Name the blood parasite species.
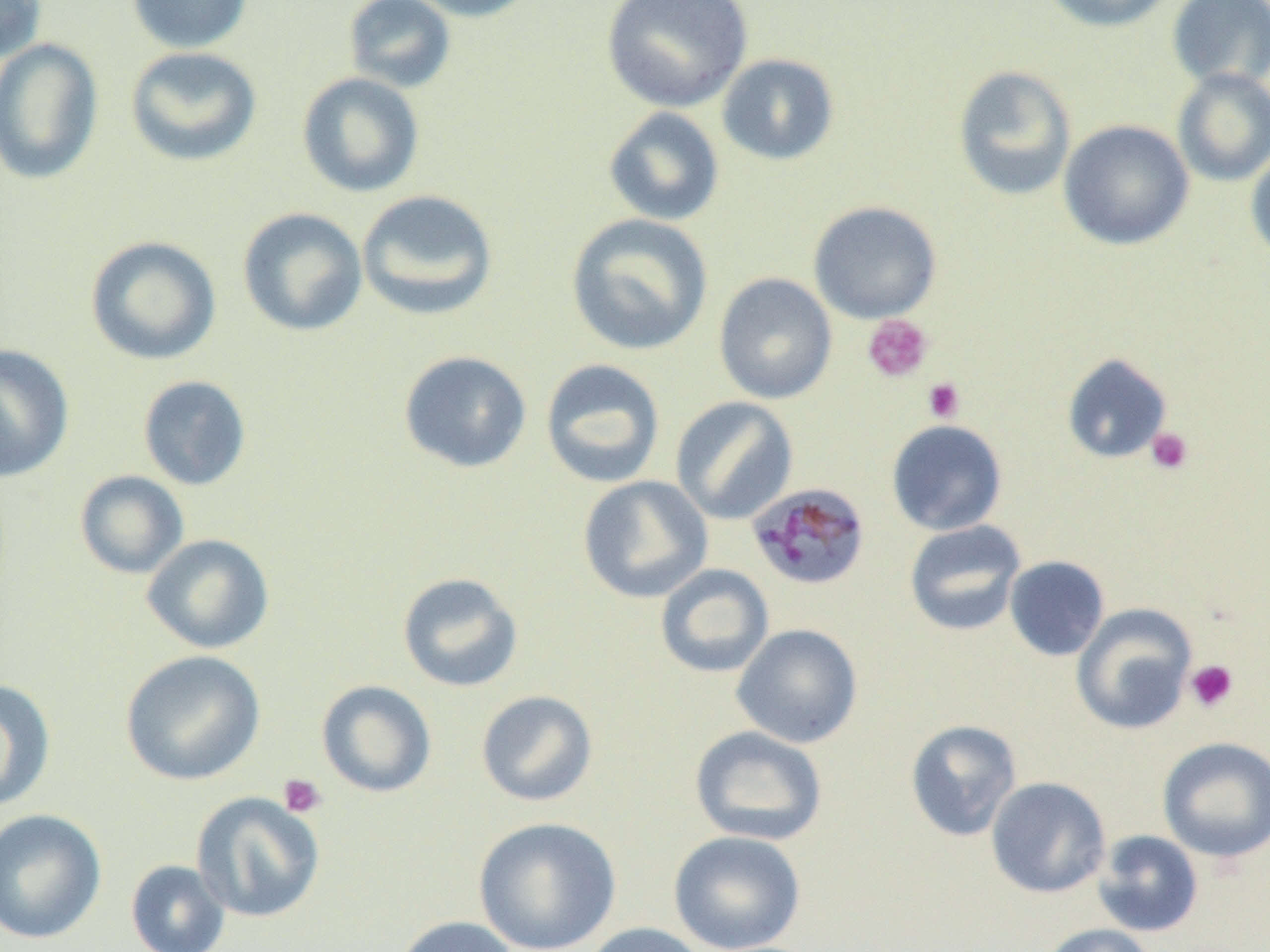
Plasmodium malariae.

Summary:
  - Coordinate format: approximate bounding boxes as (x1, y1, x2, y2) in pixels
  - Uninfected red blood cell locations: (0, 0, 47, 62), (127, 0, 252, 54), (342, 0, 457, 93), (407, 0, 541, 22), (601, 0, 753, 112), (1038, 0, 1175, 32), (1167, 0, 1270, 91), (0, 39, 104, 185), (125, 46, 262, 167), (717, 53, 840, 166), (952, 64, 1077, 201), (1172, 68, 1270, 187), (297, 72, 425, 198), (603, 107, 724, 226), (1058, 119, 1194, 251), (1246, 145, 1270, 265), (356, 189, 498, 321), (808, 200, 942, 324), (237, 207, 368, 337), (565, 213, 714, 356), (85, 235, 221, 365), (713, 272, 837, 404), (0, 344, 75, 483), (398, 350, 532, 474), (1062, 353, 1173, 464), (540, 358, 666, 488), (137, 375, 252, 491), (670, 396, 799, 525), (886, 419, 1007, 536), (74, 470, 189, 579), (577, 475, 713, 603), (904, 520, 1027, 636), (142, 534, 275, 654), (1004, 555, 1110, 662), (655, 564, 774, 679), (397, 572, 523, 693), (1071, 603, 1197, 734), (731, 623, 863, 749), (120, 650, 267, 786), (0, 678, 56, 813), (316, 680, 437, 798), (475, 690, 598, 806), (905, 719, 1022, 842), (689, 725, 828, 846), (1157, 737, 1270, 863), (985, 777, 1111, 898), (191, 791, 325, 923), (0, 808, 108, 945), (473, 816, 622, 952), (668, 830, 806, 952), (1092, 830, 1204, 938), (125, 859, 230, 952), (393, 915, 522, 952), (581, 921, 711, 952), (1039, 923, 1159, 952)
  - Platelet locations: (862, 314, 933, 382), (923, 378, 965, 422), (1146, 427, 1194, 475), (1185, 659, 1239, 713), (278, 773, 327, 818)
  - Plasmodium malariae-infected red blood cell locations: (747, 482, 871, 591)
  - Preparation: thin blood smear
  - Modality: light microscopy
  - Image size: 1270×952 pixels
  - Magnification: 1000x
  - Field of view: one of a larger specimen